Classify this cell by malaria status.
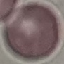

It is uninfected.

Acquired by smartphone through the microscope eyepiece. Cell patch, automatically extracted from a larger field of view and resized to 64 × 64 pixels. Giemsa stain. Thin blood film.